Identify the parasite.
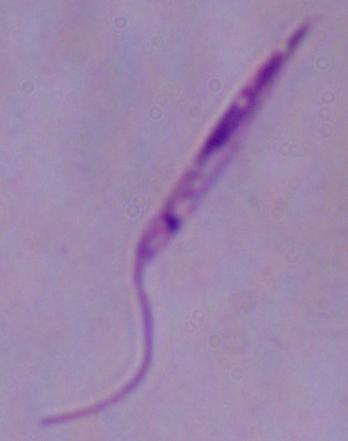
Leishmania.

Micrograph. Captured at 1000x magnification.